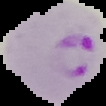

Summary:
  - Image type: cell region segmented out of the field of view; surrounding area masked to black
  - Result: Plasmodium parasites identified
  - Image size: 106×106 pixels
  - Preparation: thin blood smear